Assess the morphology of the red blood cells.
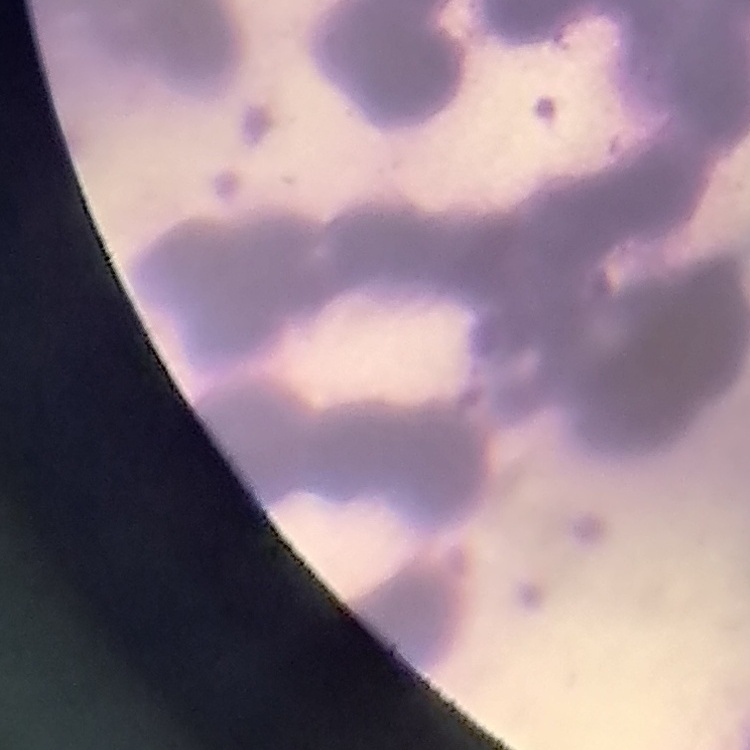

Rouleaux formation.

Summary:
  - Stain: Field's or Giemsa
  - Preparation: thin blood smear
  - Image type: square crop of a larger photomicrograph